Locate and identify every blood parasite.
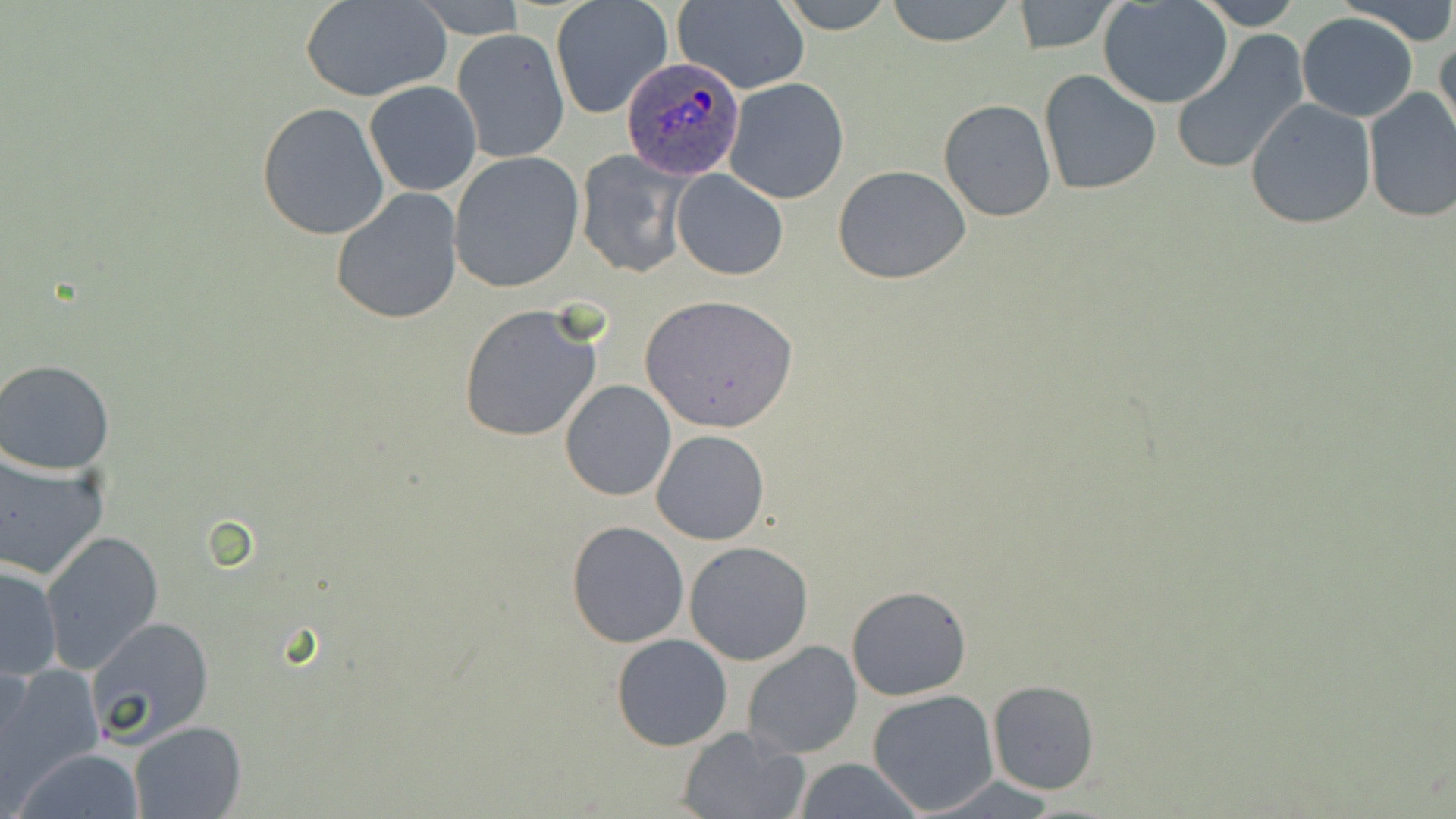
Approximate bounding boxes as (x1, y1, x2, y2) in pixels.
Plasmodium ovale-infected red blood cells: (620, 56, 748, 179).
No Plasmodium falciparum, Plasmodium malariae, Plasmodium vivax, Babesia divergens, or Trypanosoma brucei observed.

Summary:
  - Uninfected red blood cell locations: (301, 0, 451, 103), (775, 0, 899, 33), (884, 0, 1020, 48), (1188, 0, 1305, 31), (1334, 0, 1456, 44), (551, 1, 674, 120), (672, 1, 810, 93), (1011, 1, 1120, 54), (1098, 1, 1235, 109), (1297, 13, 1419, 122), (452, 29, 569, 162), (1171, 31, 1309, 176), (1434, 31, 1456, 151), (1039, 70, 1162, 193), (723, 78, 851, 204), (364, 81, 482, 197), (1362, 86, 1456, 224), (1245, 97, 1376, 229), (938, 99, 1055, 221), (257, 102, 391, 240), (449, 151, 585, 293), (576, 151, 688, 278), (831, 164, 972, 284), (672, 169, 788, 280), (330, 187, 463, 324), (639, 293, 800, 435), (459, 304, 605, 444), (0, 359, 118, 474), (558, 379, 676, 502), (651, 428, 770, 545), (0, 450, 108, 582), (567, 521, 688, 647), (40, 531, 163, 674), (684, 540, 815, 666), (1, 562, 63, 681), (845, 584, 971, 701), (86, 615, 215, 747), (610, 634, 733, 751), (742, 639, 862, 759), (1, 664, 101, 793), (987, 680, 1099, 795), (866, 689, 1000, 815), (129, 720, 246, 819), (676, 726, 809, 819), (14, 747, 146, 819), (791, 757, 922, 819)
  - Slide-level diagnosis: Plasmodium ovale
  - Stain: May-Grünwald-Giemsa
  - Field of view: one of a larger specimen
  - Modality: optical microscopy
  - Image size: 1456×819 pixels
  - Magnification: 1000x
  - Preparation: thin blood smear